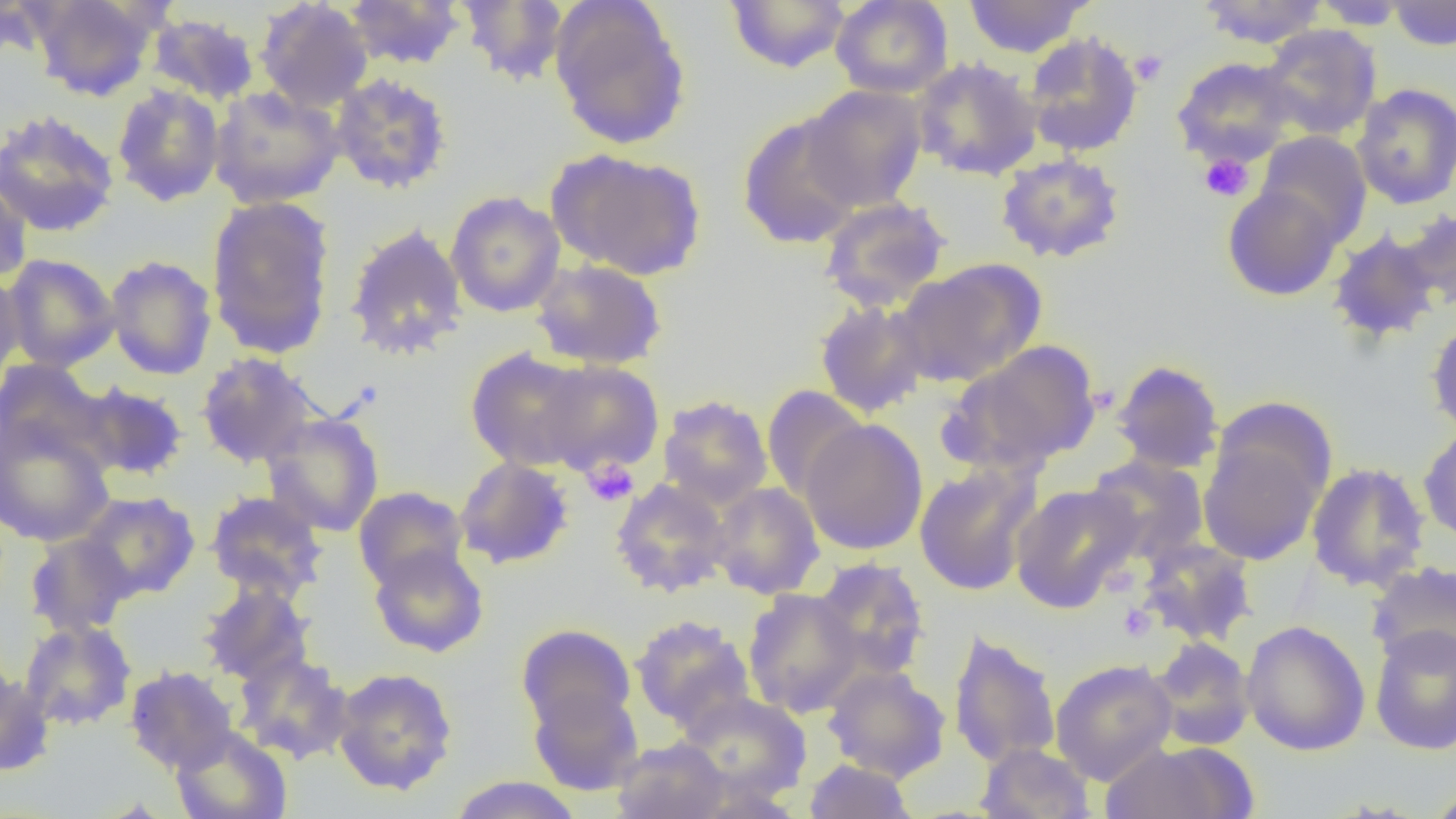

slide-level diagnosis = negative for blood parasites
modality = optical microscopy
field of view = one of a larger specimen
uninfected red blood cell locations = approximate bounding boxes as named x1/y1/x2/y2 corners in pixels: (x1=0, y1=0, x2=50, y2=64), (x1=29, y1=0, x2=163, y2=101), (x1=342, y1=0, x2=468, y2=70), (x1=548, y1=0, x2=691, y2=151), (x1=830, y1=0, x2=954, y2=99), (x1=962, y1=0, x2=1094, y2=58), (x1=1195, y1=0, x2=1330, y2=48), (x1=254, y1=1, x2=374, y2=111), (x1=457, y1=1, x2=569, y2=86), (x1=724, y1=1, x2=851, y2=74), (x1=1309, y1=1, x2=1414, y2=29), (x1=1387, y1=1, x2=1455, y2=51), (x1=147, y1=11, x2=261, y2=106), (x1=1259, y1=24, x2=1382, y2=140), (x1=1022, y1=32, x2=1143, y2=158), (x1=1171, y1=56, x2=1301, y2=167), (x1=912, y1=57, x2=1044, y2=181), (x1=329, y1=73, x2=454, y2=194), (x1=1352, y1=83, x2=1456, y2=210), (x1=112, y1=84, x2=225, y2=207), (x1=801, y1=84, x2=928, y2=211), (x1=208, y1=85, x2=346, y2=209), (x1=0, y1=109, x2=120, y2=238), (x1=737, y1=112, x2=865, y2=250), (x1=1256, y1=131, x2=1372, y2=247), (x1=548, y1=148, x2=707, y2=281), (x1=995, y1=152, x2=1126, y2=263), (x1=0, y1=172, x2=33, y2=284), (x1=1222, y1=183, x2=1343, y2=301), (x1=445, y1=191, x2=565, y2=318), (x1=205, y1=195, x2=337, y2=358), (x1=818, y1=196, x2=952, y2=312), (x1=1397, y1=207, x2=1456, y2=313), (x1=345, y1=223, x2=468, y2=360), (x1=1327, y1=228, x2=1442, y2=345), (x1=2, y1=253, x2=120, y2=372), (x1=104, y1=255, x2=217, y2=380), (x1=531, y1=259, x2=667, y2=369), (x1=895, y1=259, x2=1046, y2=387), (x1=0, y1=270, x2=26, y2=386), (x1=814, y1=299, x2=932, y2=417), (x1=1426, y1=314, x2=1456, y2=439), (x1=953, y1=341, x2=1102, y2=471), (x1=465, y1=348, x2=597, y2=471), (x1=196, y1=352, x2=318, y2=469), (x1=0, y1=358, x2=106, y2=464), (x1=1111, y1=359, x2=1226, y2=474), (x1=533, y1=360, x2=665, y2=475), (x1=74, y1=382, x2=190, y2=480), (x1=761, y1=385, x2=869, y2=501), (x1=657, y1=395, x2=773, y2=510), (x1=262, y1=413, x2=384, y2=537), (x1=0, y1=416, x2=115, y2=547), (x1=800, y1=418, x2=928, y2=554), (x1=1198, y1=424, x2=1329, y2=567), (x1=1418, y1=424, x2=1456, y2=545), (x1=1085, y1=454, x2=1210, y2=563), (x1=454, y1=456, x2=574, y2=570), (x1=912, y1=461, x2=1043, y2=597), (x1=1306, y1=462, x2=1430, y2=592), (x1=610, y1=477, x2=731, y2=598), (x1=708, y1=482, x2=825, y2=599), (x1=1010, y1=483, x2=1143, y2=612), (x1=353, y1=486, x2=469, y2=591), (x1=77, y1=491, x2=201, y2=601), (x1=205, y1=491, x2=328, y2=602), (x1=24, y1=532, x2=136, y2=637), (x1=1137, y1=538, x2=1258, y2=648), (x1=368, y1=544, x2=489, y2=658), (x1=812, y1=558, x2=930, y2=680), (x1=1366, y1=561, x2=1456, y2=671), (x1=198, y1=581, x2=314, y2=685), (x1=742, y1=588, x2=865, y2=717), (x1=629, y1=614, x2=756, y2=734), (x1=19, y1=619, x2=137, y2=730), (x1=1241, y1=620, x2=1371, y2=756), (x1=516, y1=623, x2=636, y2=733), (x1=1369, y1=624, x2=1456, y2=756), (x1=948, y1=629, x2=1062, y2=769), (x1=1147, y1=638, x2=1256, y2=750), (x1=233, y1=652, x2=353, y2=764), (x1=1050, y1=658, x2=1178, y2=786), (x1=124, y1=664, x2=238, y2=774), (x1=822, y1=664, x2=951, y2=783), (x1=332, y1=666, x2=458, y2=796), (x1=0, y1=670, x2=55, y2=776), (x1=528, y1=684, x2=644, y2=796), (x1=675, y1=692, x2=813, y2=802), (x1=171, y1=726, x2=292, y2=819), (x1=610, y1=736, x2=731, y2=819), (x1=1099, y1=741, x2=1256, y2=818), (x1=976, y1=742, x2=1096, y2=818), (x1=804, y1=759, x2=917, y2=818), (x1=448, y1=775, x2=583, y2=819), (x1=1423, y1=783, x2=1456, y2=818)
magnification = 1000x
preparation = thin blood film
platelet locations = approximate bounding boxes as named x1/y1/x2/y2 corners in pixels: (x1=1129, y1=50, x2=1168, y2=86), (x1=1199, y1=153, x2=1255, y2=202), (x1=582, y1=459, x2=639, y2=507), (x1=1117, y1=603, x2=1156, y2=642)
image size = 1456×819 pixels